State which parasite is depicted.
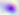

Toxoplasma gondii.

modality = photomicrograph
magnification = 400x